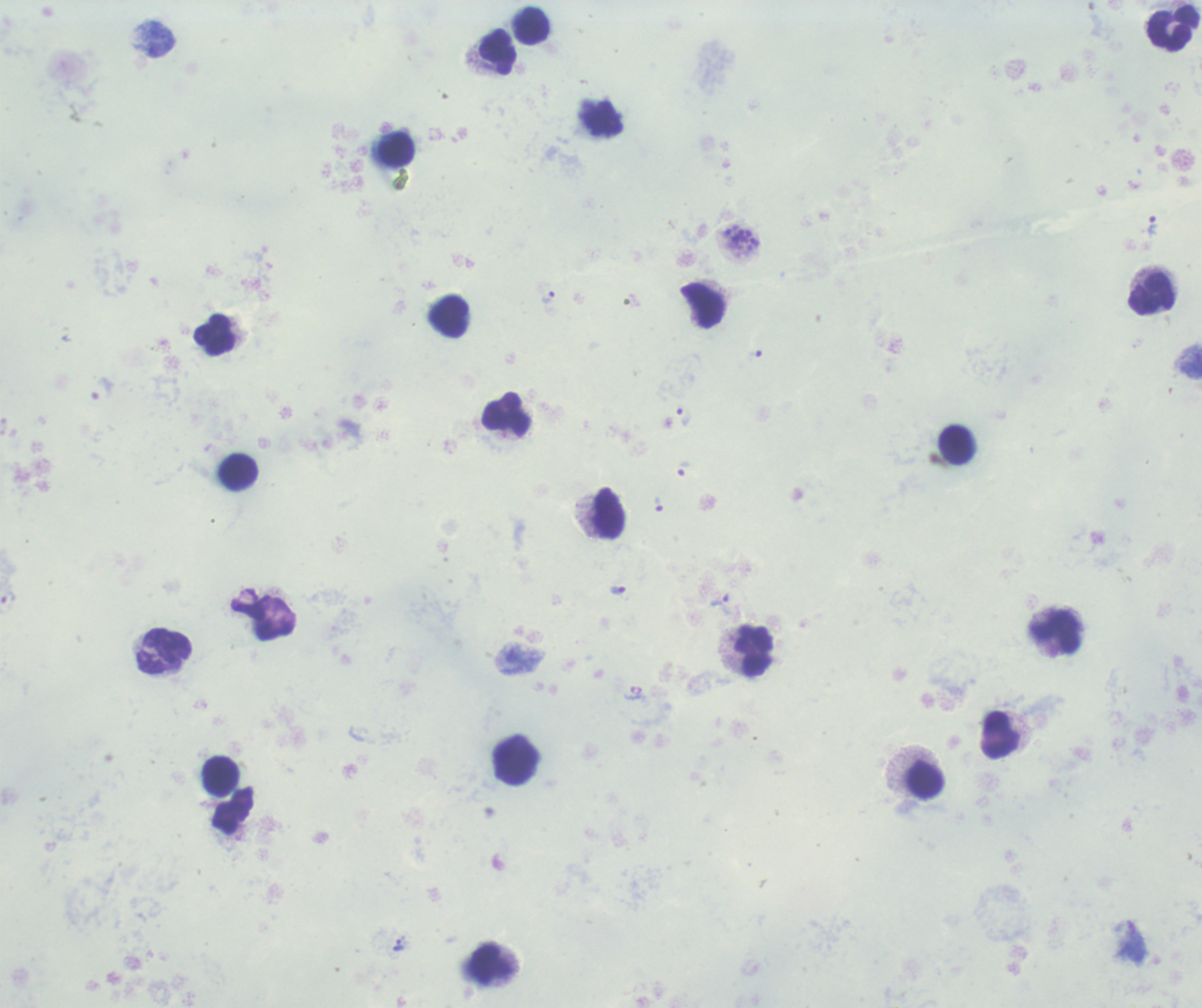

Approximate centers as [x, y] in pixels. Trophozoite locations: [1153, 226], [548, 298], [100, 389], [683, 415], [683, 468], [658, 504], [617, 590], [721, 604], [398, 945]. Leukocyte locations: [532, 26], [1174, 27], [498, 52], [602, 118], [397, 149], [1151, 294], [703, 306], [449, 316], [214, 335], [506, 415], [957, 445], [239, 472], [608, 513], [1055, 633], [165, 651], [755, 651], [1000, 735], [517, 760], [221, 775], [926, 780], [490, 963]. Schizont locations: [742, 241]. Life-cycle stages observed: trophozoite, schizont. Thick smear of blood. Romanowsky-stained preparation. Result: positive for Plasmodium parasites. Previously used in a real diagnosis. Captured at 100x magnification. One field from this slide. Image is 1202×1008 pixels. Background quality: unsatisfactory.